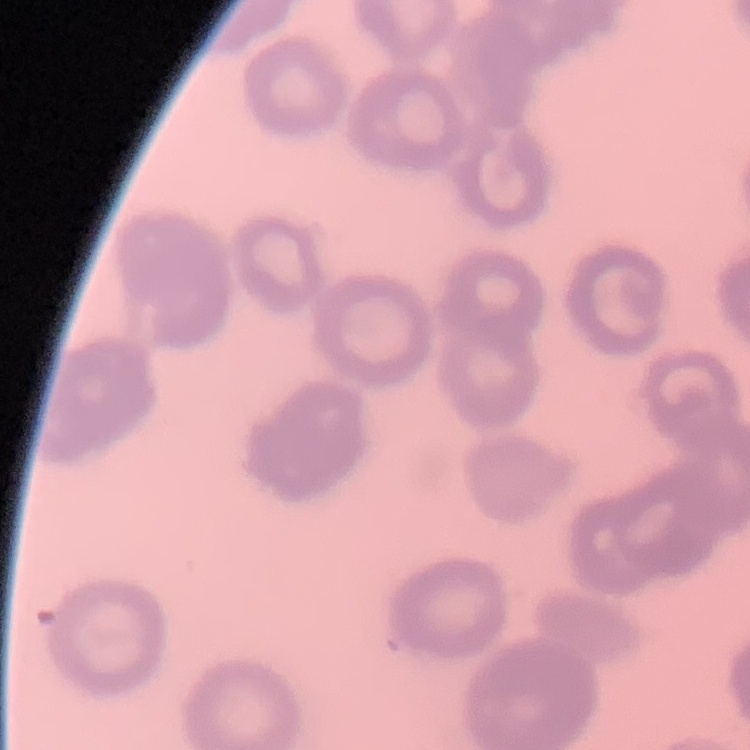

The red blood cells exhibit rouleaux formation. One tile cut from a larger photomicrograph. Thin peripheral smear. Field's or Giemsa stain.